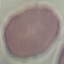
{
  "result": "no malaria parasites seen",
  "stain": "Giemsa",
  "image_type": "automatically extracted cell patch, resized to 64 × 64 pixels",
  "capture": "smartphone camera at the microscope eyepiece",
  "preparation": "thin smear"
}